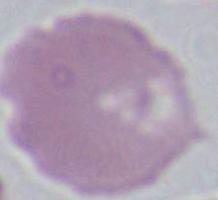
Summary:
  - Identification: erythrocyte
  - Magnification: 1000x
  - Modality: micrograph